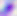

Photomicrograph. Toxoplasma gondii is seen. Captured at 400x magnification.